Classify this cell by malaria status.
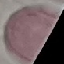

It is uninfected.

image type = cell patch, automatically extracted from a larger field of view and resized to 64 × 64 pixels
preparation = thin smear
stain = Giemsa
capture = smartphone camera at the microscope eyepiece